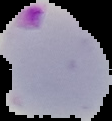

Summary:
  - Preparation: thin blood smear
  - Image size: 112×121 pixels
  - Result: Plasmodium parasites detected
  - Image type: segmented cell region with the area outside set to black